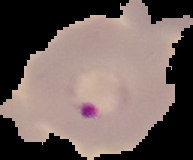

Summary:
  - Image type: cell region segmented out of the field of view; surrounding area masked to black
  - Preparation: thin blood smear
  - Image size: 193×160 pixels
  - Result: malaria parasites detected